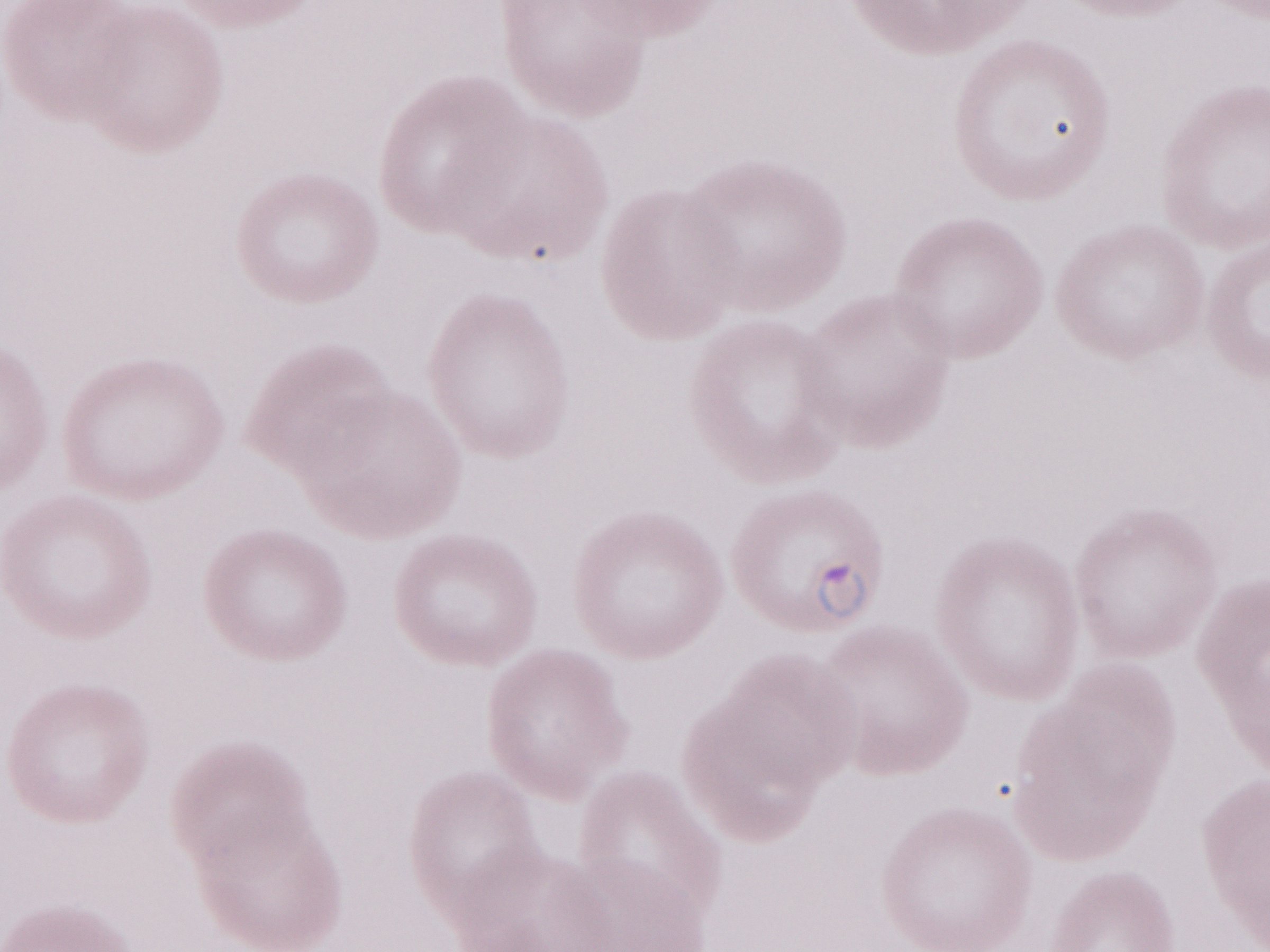

Patient diagnosis: malaria infection. 1,000x magnification. Single field of view. Olympus BX43 microscope, Olympus DP73 camera. Image is 1270×952 pixels. May-Grünwald-Giemsa-stained preparation. Thin blood smear.